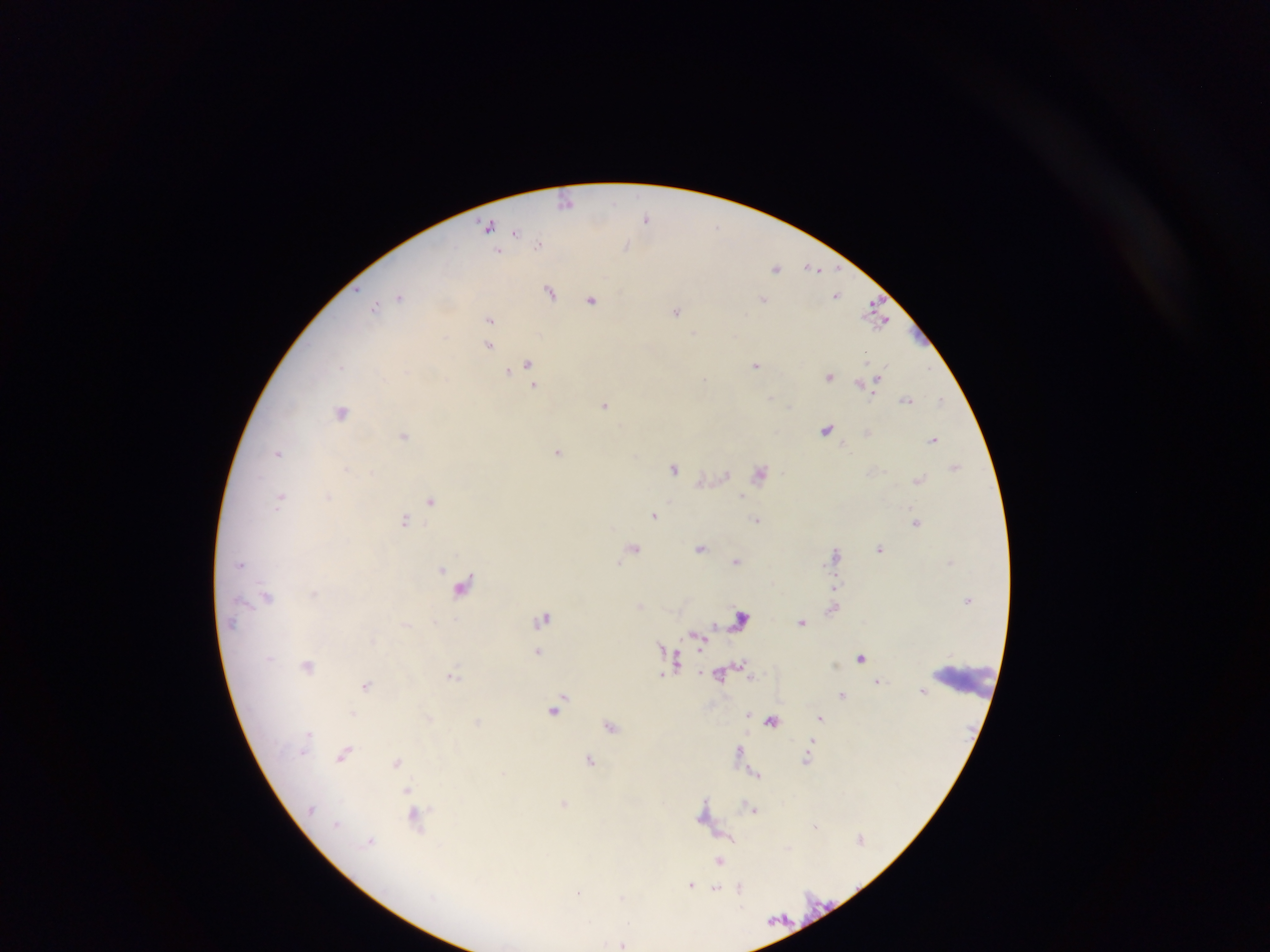

preparation = thick blood smear
image size = 1270×952 pixels
malaria parasite locations = approximate centers as (x, y) in pixels: (565, 198), (646, 218), (487, 225), (719, 225), (514, 231), (538, 243), (625, 246), (497, 251), (776, 268), (808, 268), (816, 268), (548, 292), (837, 295), (401, 296), (764, 298), (592, 300), (869, 306), (375, 307), (676, 311), (490, 319), (882, 322), (695, 332), (488, 346), (868, 356), (528, 362), (756, 365), (341, 367), (510, 370), (830, 376), (705, 378), (878, 379), (860, 382), (536, 385), (905, 399), (942, 400), (607, 405), (342, 413), (826, 430), (403, 436), (933, 440), (559, 452), (277, 453), (956, 464), (674, 468), (347, 469), (761, 474), (726, 475), (920, 479), (328, 496), (744, 497), (281, 498), (432, 501), (655, 515), (405, 520), (757, 520), (916, 522), (634, 547), (880, 547), (702, 549), (836, 554), (736, 561), (620, 563), (442, 569), (837, 581), (464, 585), (266, 597), (640, 606), (833, 609), (741, 618), (545, 619), (802, 623), (695, 634), (662, 647), (537, 652), (673, 652), (677, 658), (862, 658), (834, 663), (308, 664), (740, 665), (454, 675), (367, 686), (924, 691), (842, 694), (561, 704), (750, 710), (353, 714), (748, 714), (820, 717), (771, 721), (612, 725), (306, 737), (812, 742), (740, 748), (304, 752), (344, 754), (591, 758), (806, 759), (397, 761), (756, 775), (406, 789), (706, 799), (565, 802), (704, 807), (754, 811), (702, 815), (413, 817), (335, 821), (813, 826), (728, 836), (370, 839), (788, 847), (720, 861), (691, 884), (716, 888), (740, 891), (579, 893), (624, 897), (623, 943)
field of view = single
country = Ghana
capture = mobile-phone photograph through a microscope